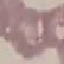
{
  "malaria_status": "uninfected",
  "capture": "smartphone camera at the microscope eyepiece",
  "stain": "Giemsa",
  "preparation": "thin blood film",
  "image_type": "cell patch, automatically extracted from a larger field of view and resized to 64 × 64 pixels"
}